Classify this cell by malaria status.
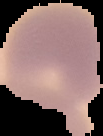
It is uninfected.

Image is 103×136 pixels. Segmented cell region on a black background. From a thin blood film.